Locate and identify every blood parasite.
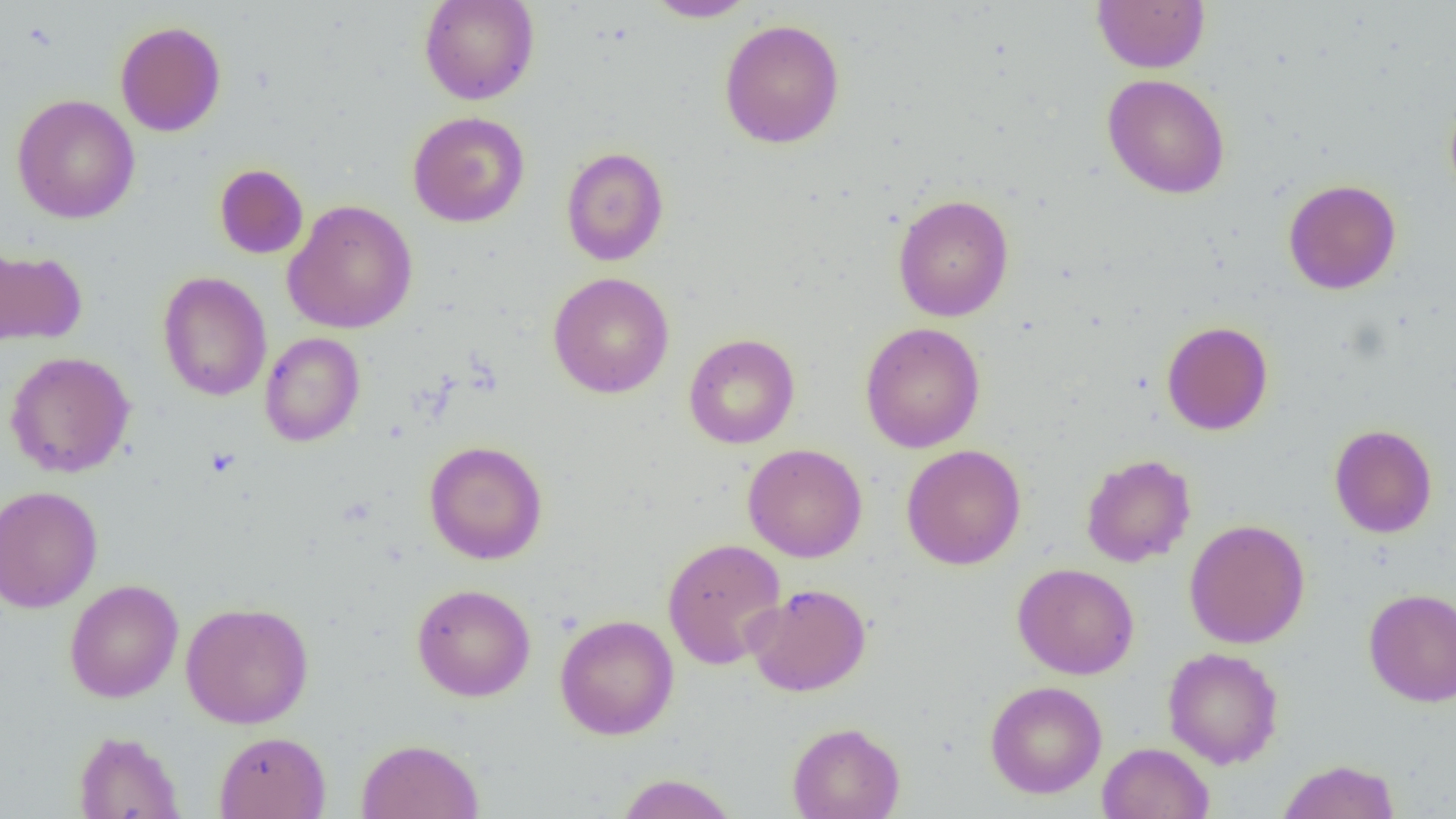
No blood parasites observed.

{
  "slide_level_diagnosis": "negative for blood parasites",
  "preparation": "thin blood smear",
  "magnification": "1000x",
  "field_of_view": "single",
  "uninfected_red_blood_cell_locations": "approximate bounding boxes as named x1/y1/x2/y2 corners in pixels: (x1=418, y1=0, x2=540, y2=105), (x1=643, y1=0, x2=757, y2=22), (x1=1091, y1=0, x2=1211, y2=74), (x1=719, y1=18, x2=845, y2=148), (x1=115, y1=21, x2=226, y2=137), (x1=1102, y1=74, x2=1230, y2=199), (x1=1444, y1=86, x2=1456, y2=205), (x1=12, y1=94, x2=140, y2=224), (x1=407, y1=111, x2=530, y2=227), (x1=560, y1=147, x2=669, y2=266), (x1=214, y1=164, x2=308, y2=259), (x1=1283, y1=178, x2=1402, y2=294), (x1=892, y1=193, x2=1014, y2=322), (x1=282, y1=200, x2=418, y2=334), (x1=0, y1=246, x2=87, y2=349), (x1=157, y1=271, x2=272, y2=402), (x1=548, y1=271, x2=674, y2=399), (x1=1161, y1=320, x2=1273, y2=435), (x1=860, y1=322, x2=986, y2=452), (x1=260, y1=332, x2=365, y2=447), (x1=683, y1=333, x2=800, y2=449), (x1=5, y1=351, x2=135, y2=477), (x1=1329, y1=424, x2=1438, y2=538), (x1=423, y1=440, x2=548, y2=565), (x1=742, y1=443, x2=868, y2=562), (x1=901, y1=443, x2=1026, y2=570), (x1=1080, y1=453, x2=1196, y2=567), (x1=0, y1=485, x2=103, y2=612), (x1=1184, y1=519, x2=1310, y2=648), (x1=662, y1=537, x2=787, y2=670), (x1=1012, y1=562, x2=1139, y2=680), (x1=64, y1=579, x2=183, y2=703), (x1=412, y1=583, x2=536, y2=702), (x1=744, y1=583, x2=872, y2=697), (x1=1363, y1=588, x2=1456, y2=707), (x1=180, y1=601, x2=314, y2=728), (x1=555, y1=614, x2=679, y2=740), (x1=1162, y1=647, x2=1284, y2=769), (x1=985, y1=680, x2=1107, y2=798), (x1=786, y1=722, x2=905, y2=819), (x1=73, y1=730, x2=186, y2=818), (x1=214, y1=730, x2=331, y2=818), (x1=356, y1=738, x2=484, y2=818), (x1=1098, y1=742, x2=1214, y2=819), (x1=1276, y1=759, x2=1400, y2=819), (x1=615, y1=772, x2=739, y2=818)",
  "image_size": "1456×819 pixels",
  "modality": "optical microscopy"
}